Report the malaria status of this cell.
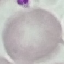

Uninfected.

Summary:
  - Image type: cell patch, automatically extracted from a larger field of view and resized to 64 × 64 pixels
  - Stain: Giemsa
  - Capture: smartphone camera at the microscope eyepiece
  - Preparation: thin blood film